Comment on the morphology of the red blood cells.
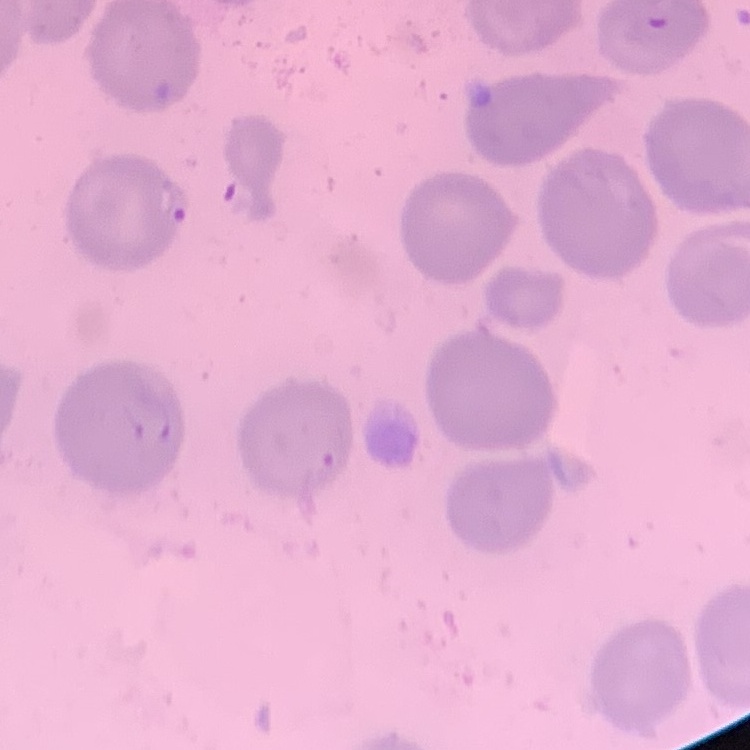
They show no rouleaux formation.

Summary:
  - Image type: square crop of a larger photomicrograph
  - Preparation: thin blood film
  - Stain: Field's or Giemsa